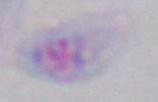 Micrograph. Toxoplasma gondii is seen. Captured at 1000x magnification.